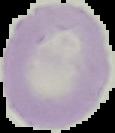

{
  "image_size": "115×133 pixels",
  "result": "no malaria parasites seen",
  "preparation": "thin blood film",
  "image_type": "segmented cell region on a black background"
}